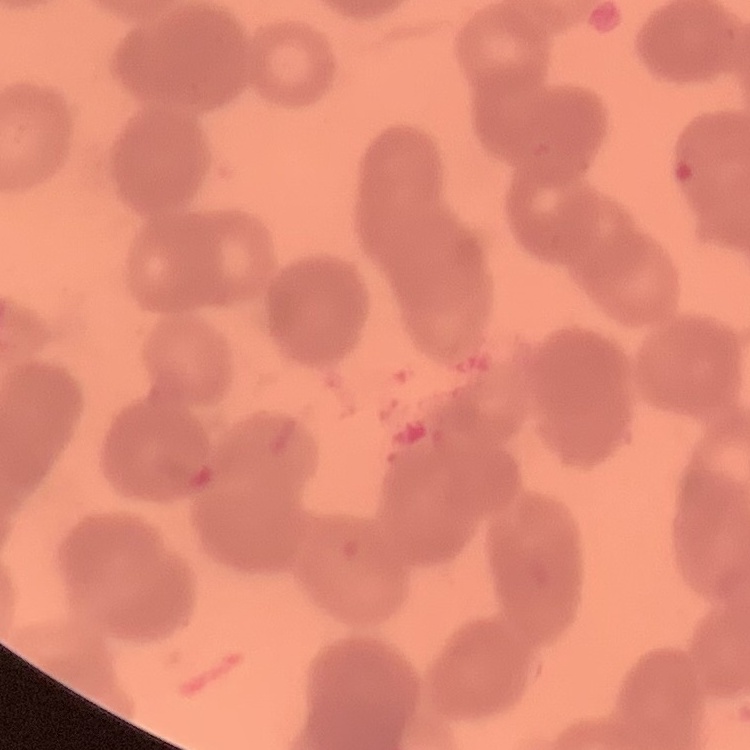

red blood cell morphology = rouleaux formation
stain = Field's or Giemsa
image type = one tile cut from a larger photomicrograph
preparation = thin peripheral smear